Name the parasite shown.
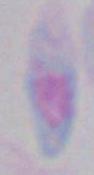
This is Toxoplasma gondii.

1000x magnification. Micrograph.